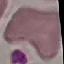 Result: no malaria parasites detected. Giemsa-stained preparation. Cell patch, automatically extracted from a larger field of view and resized to 64 × 64 pixels. Photographed with a smartphone camera at the microscope eyepiece. Thin smear of blood.